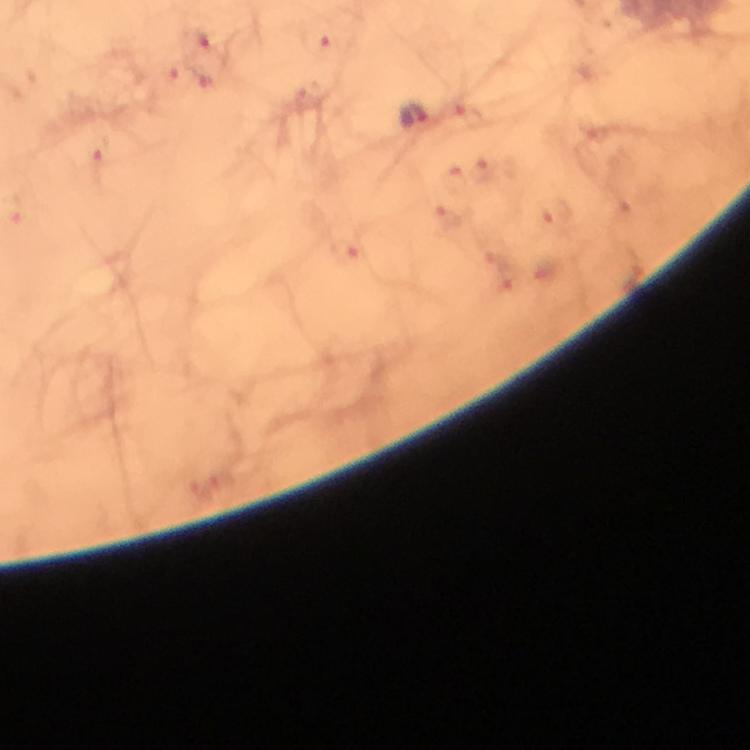

Approximate centers as {x, y} in pixels.
Summary:
  - Malaria parasite locations: {203, 38}, {322, 45}, {180, 79}, {413, 114}, {467, 114}, {98, 153}, {482, 170}, {455, 177}, {556, 216}, {448, 218}
  - Context: from a malaria diagnostic workup
  - Cropped from: one field of view
  - Stain: Giemsa
  - Capture: smartphone mounted on the microscope
  - Magnification: 100x
  - Immersion oil: applied
  - Image size: 750×750 pixels
  - Preparation: thick blood smear